Report the malaria status of this cell.
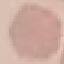

Uninfected.

Thin blood smear. Photographed with a smartphone camera at the microscope eyepiece. Automatically extracted cell patch, resized to 64 × 64 pixels. Giemsa stain.